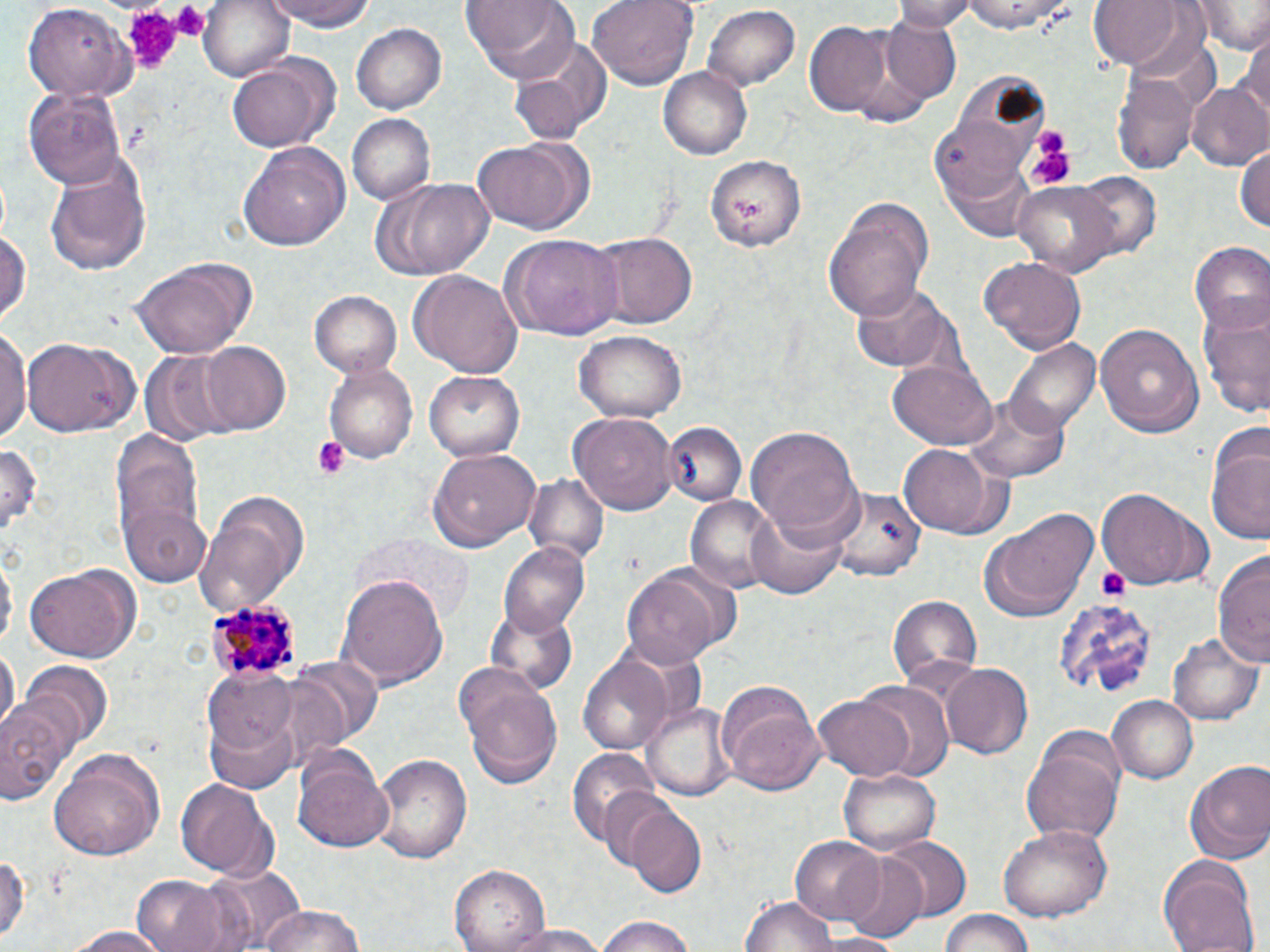

{
  "slide_level_diagnosis": "Plasmodium malariae",
  "magnification": "1000x",
  "uninfected_red_blood_cell_locations": "approximate bounding boxes as [x1, y1, x2, y2] in pixels: [196, 0, 296, 83], [262, 0, 378, 34], [460, 0, 579, 78], [587, 0, 697, 89], [890, 0, 977, 31], [958, 0, 1078, 34], [1193, 0, 1269, 54], [1089, 1, 1186, 70], [703, 3, 800, 91], [24, 4, 135, 103], [880, 18, 961, 102], [804, 22, 893, 117], [353, 24, 445, 115], [1240, 29, 1270, 126], [509, 35, 614, 140], [227, 56, 335, 153], [658, 68, 752, 161], [1115, 72, 1197, 177], [1186, 81, 1270, 173], [24, 87, 127, 191], [345, 112, 434, 205], [470, 136, 593, 235], [239, 141, 349, 253], [1234, 143, 1270, 237], [706, 151, 804, 251], [43, 153, 152, 277], [1073, 171, 1160, 260], [370, 177, 495, 281], [1013, 181, 1123, 279], [826, 200, 933, 318], [0, 222, 29, 331], [595, 231, 695, 327], [499, 234, 624, 342], [1188, 243, 1270, 340], [129, 257, 261, 360], [980, 258, 1085, 352], [411, 269, 522, 381], [849, 282, 959, 374], [309, 290, 402, 376], [1196, 303, 1270, 421], [1094, 320, 1204, 436], [0, 326, 30, 448], [574, 329, 684, 422], [24, 339, 138, 436], [197, 340, 292, 437], [1009, 340, 1100, 437], [140, 353, 234, 445], [888, 360, 996, 449], [325, 361, 418, 464], [424, 368, 527, 460], [964, 396, 1068, 483], [570, 412, 677, 515], [664, 421, 744, 506], [747, 425, 862, 543], [1206, 428, 1270, 545], [110, 434, 211, 578], [0, 438, 41, 539], [898, 443, 1009, 538], [428, 446, 541, 551], [523, 474, 608, 565], [831, 485, 925, 580], [1094, 487, 1210, 590], [194, 489, 309, 611], [687, 495, 781, 595], [122, 503, 214, 585], [744, 506, 852, 598], [984, 506, 1099, 619], [499, 542, 590, 633], [1, 549, 15, 655], [1214, 552, 1269, 670], [624, 563, 733, 668], [24, 566, 140, 661], [341, 574, 447, 691], [888, 594, 983, 691], [1054, 595, 1159, 703], [486, 607, 577, 693], [1167, 632, 1264, 726], [1, 643, 18, 738], [578, 651, 675, 756], [291, 657, 383, 752], [20, 663, 113, 750], [456, 664, 566, 789], [942, 664, 1034, 760], [203, 670, 297, 753], [845, 679, 955, 779], [715, 680, 826, 795], [812, 693, 919, 782], [1106, 695, 1198, 785], [1, 697, 79, 805], [645, 703, 733, 798], [205, 714, 299, 794], [1022, 745, 1123, 847], [48, 747, 165, 861], [564, 747, 662, 853], [293, 750, 395, 854], [371, 752, 471, 864], [1183, 760, 1270, 866], [839, 769, 941, 854], [175, 777, 279, 880], [624, 805, 707, 898], [998, 825, 1115, 920], [789, 836, 885, 923], [884, 836, 971, 921], [0, 848, 31, 949], [838, 851, 928, 943], [1158, 855, 1261, 952], [200, 865, 308, 949], [451, 865, 548, 952], [133, 874, 233, 952], [738, 894, 834, 952], [252, 904, 368, 952], [937, 908, 1040, 952], [590, 916, 702, 951], [500, 924, 608, 951], [61, 925, 173, 951]",
  "platelet_locations": "approximate bounding boxes as [x1, y1, x2, y2] in pixels: [166, 2, 210, 39], [118, 5, 183, 75], [1026, 135, 1077, 189], [311, 437, 351, 479], [1098, 568, 1131, 603]",
  "modality": "optical microscopy",
  "stain": "May-Grünwald-Giemsa",
  "field_of_view": "single",
  "image_size": "1270×952 pixels",
  "plasmodium_malariae_infected_red_blood_cell_locations": "approximate bounding boxes as [x1, y1, x2, y2] in pixels: [206, 594, 302, 685]",
  "preparation": "thin blood film"
}